Report the malaria status of this cell.
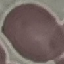

It is uninfected.

Summary:
  - Image type: cell patch, automatically extracted from a larger field of view and resized to 64 × 64 pixels
  - Stain: Giemsa
  - Preparation: thin smear
  - Capture: smartphone through the microscope eyepiece